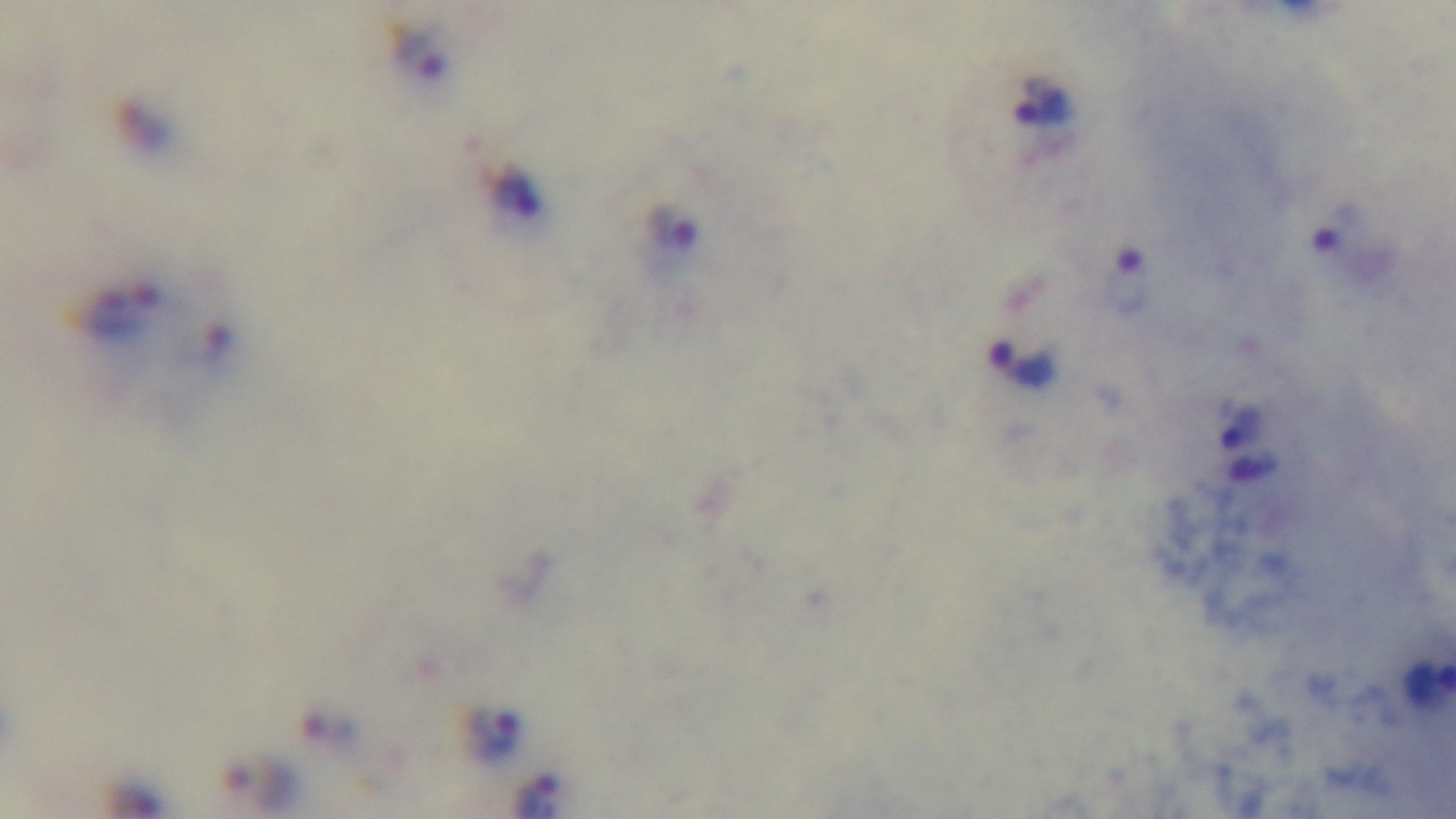 Captured with a mounted 4K digital camera. Malaria status: infected. One field from the slide. Oil-immersion objective, 100x. Giemsa-stained. Light microscopy. Preparation: thick.